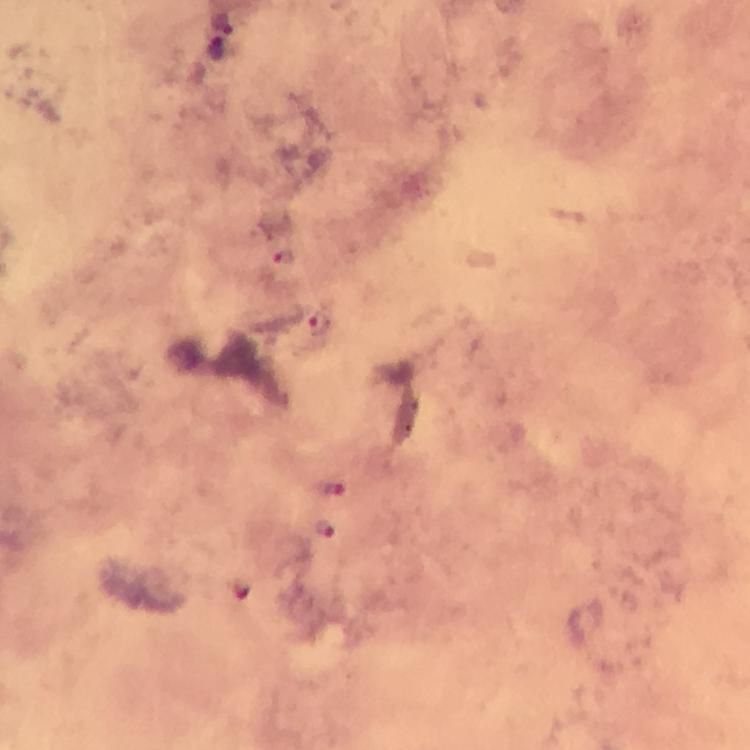
Approximate centers as [x, y] in pixels. Malaria parasite locations: [220, 38], [283, 257], [319, 323], [334, 490], [325, 528]. Giemsa-stained preparation. Photographed through the microscope with a smartphone camera. From a malaria diagnostic workup. 100x magnification. Image is 750×750 pixels. Cropped region of a single field of view. Thick blood smear. Immersion oil was used.